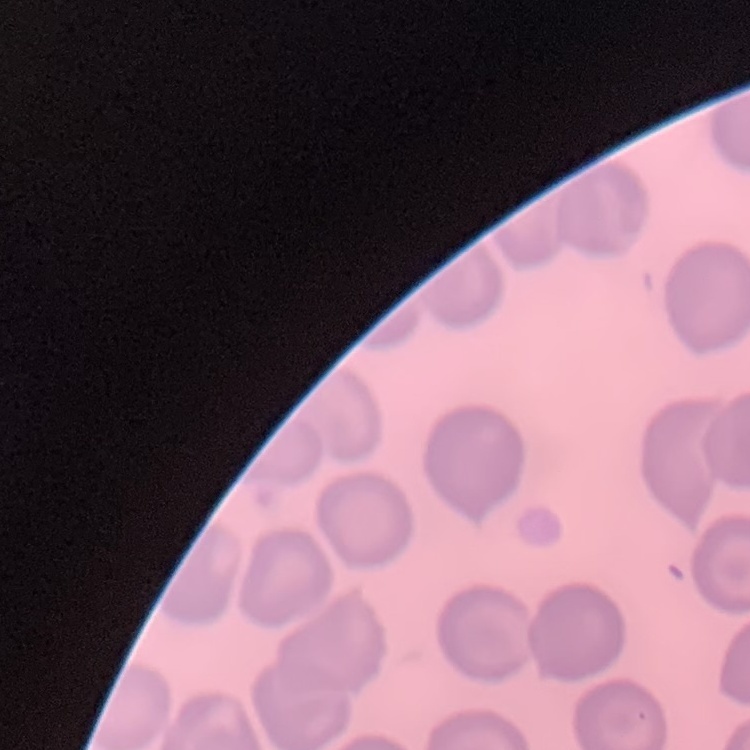

{
  "red_blood_cell_morphology": "no rouleaux formation",
  "stain": "Field's or Giemsa",
  "image_type": "square crop of a larger photomicrograph",
  "preparation": "thin blood smear"
}